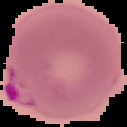

{
  "result": "malaria parasites identified",
  "image_type": "segmented cell region on a black background",
  "image_size": "127×127 pixels",
  "preparation": "thin blood film"
}